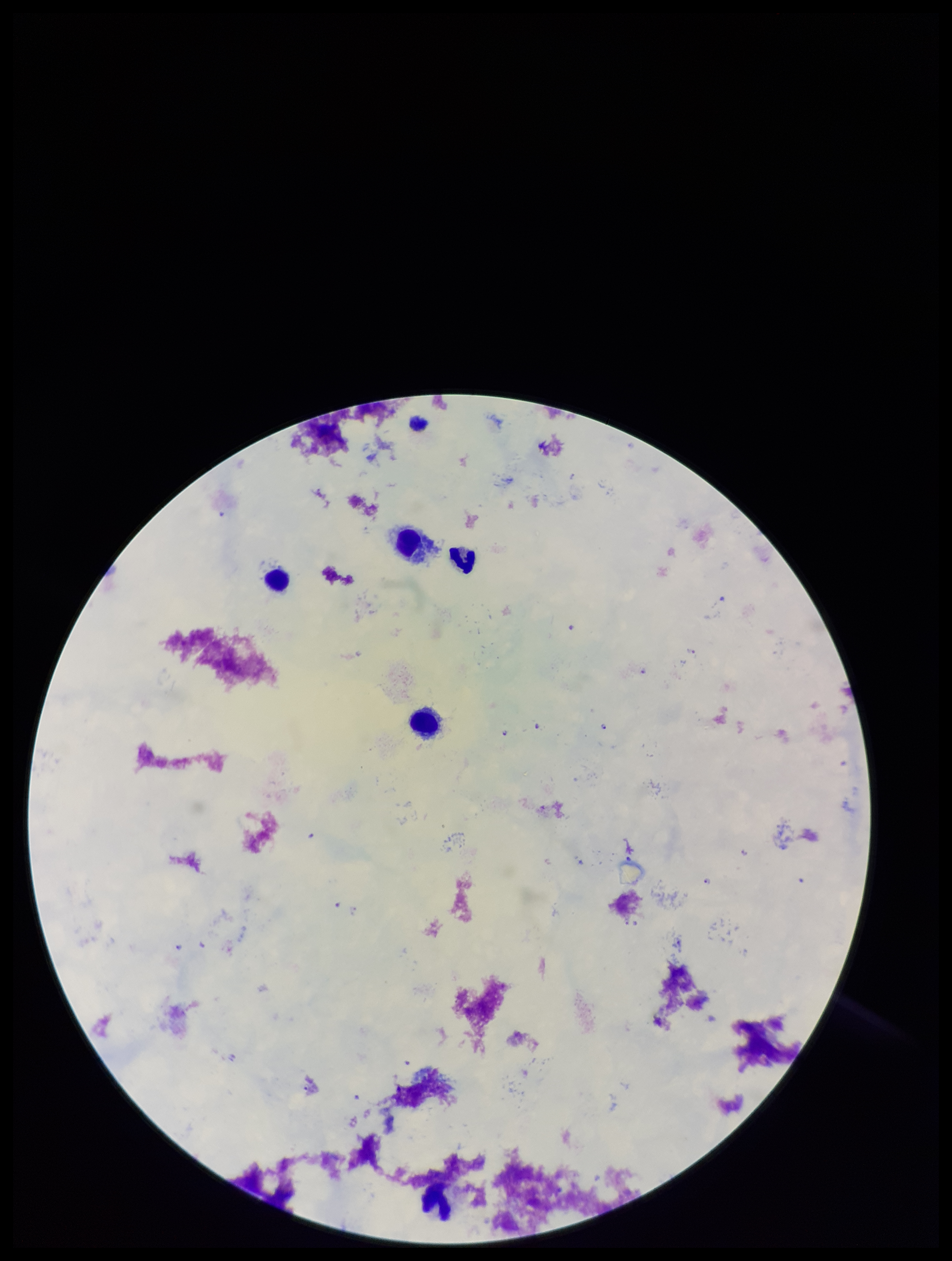
Summary:
  - Parasite count: 9
  - Plasmodium parasites: detected
  - Species reported for this patient: Plasmodium falciparum
  - Stain: Giemsa
  - Image size: 952×1261 pixels
  - Capture: smartphone photograph through the microscope eyepiece
  - Patient malaria status: positive
  - Preparation: thick smear
  - Leukocyte count: 5
  - Field of view: one from this slide